Report the malaria status of this cell.
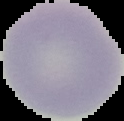
Uninfected.

Summary:
  - Preparation: thin blood film
  - Image type: segmented cell region with the area outside set to black
  - Image size: 124×121 pixels